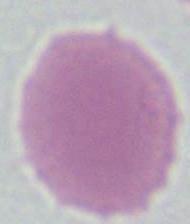
magnification = 1000x
modality = micrograph
identification = red blood cell